Comment on the morphology of the erythrocytes.
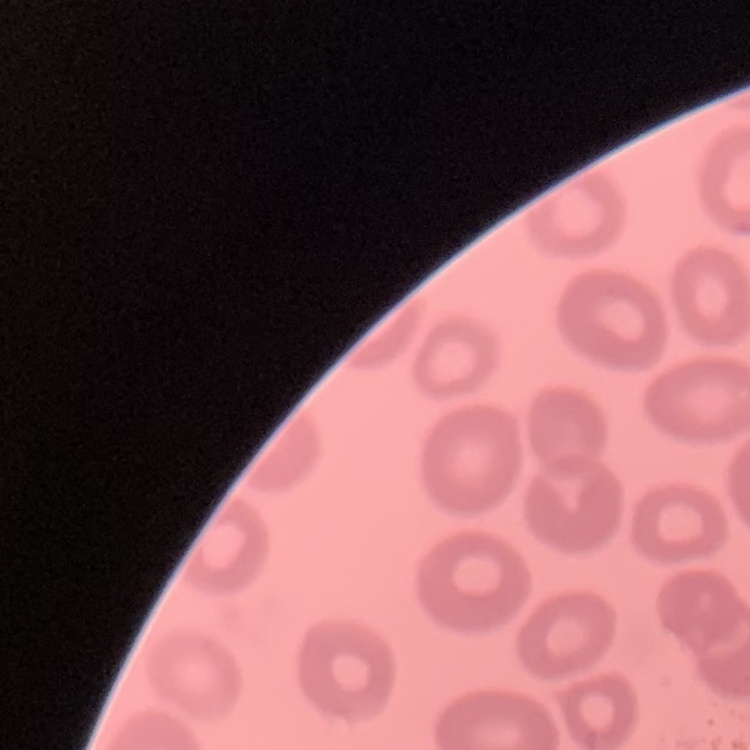

No rouleaux formation.

stain = Field's or Giemsa
image type = square crop of a larger photomicrograph
preparation = thin blood film